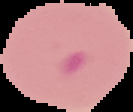

preparation: thin blood smear
image_size: 133×112 pixels
image_type: cell region segmented out of the field of view; surrounding area masked to black
result: malaria parasites detected